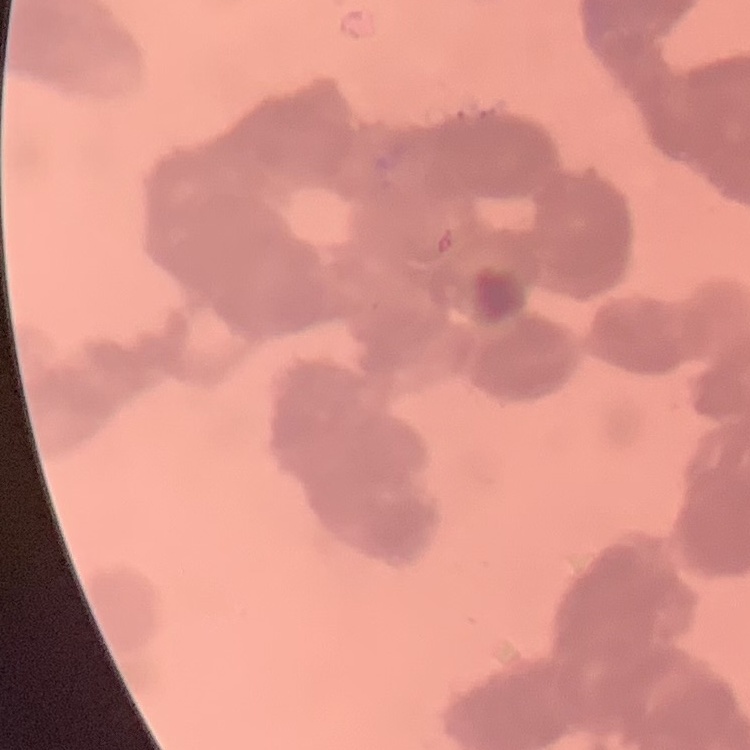 The erythrocytes exhibit rouleaux formation. One tile cut from a larger photomicrograph. Stained with either Field's or Giemsa. Thin blood film.